Assess the morphology of the erythrocytes.
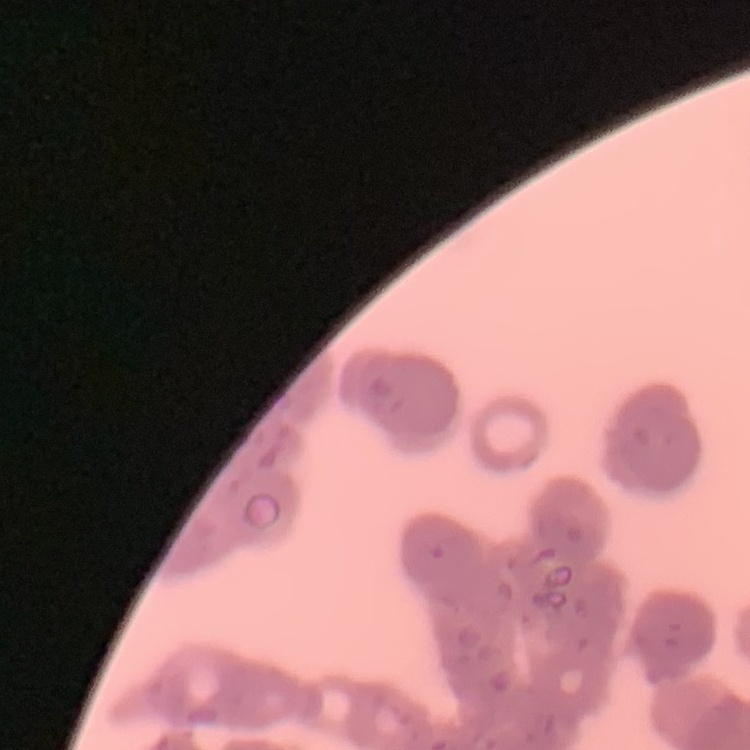
They show rouleaux formation.

Summary:
  - Preparation: thin blood smear
  - Image type: square crop of a larger photomicrograph
  - Stain: Field's or Giemsa